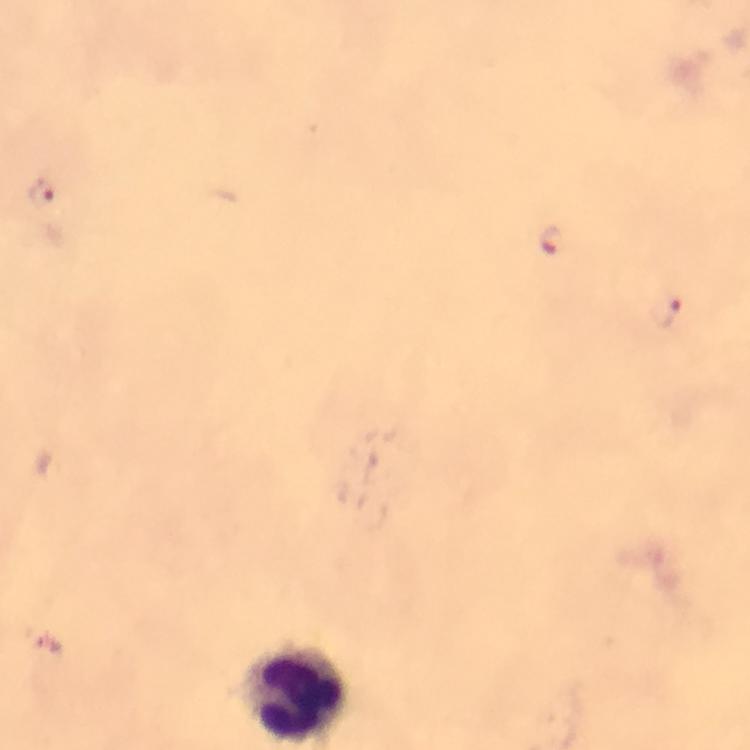

leukocyte locations = approximate object centers, in pixels from the top-left corner: (x=294, y=694)
magnification = 100x
immersion oil = used
Plasmodium parasite locations = approximate object centers, in pixels from the top-left corner: (x=40, y=190), (x=550, y=243), (x=666, y=310)
capture = smartphone photograph through a microscope
preparation = thick blood film
context = from a malaria diagnostic workup
stain = Giemsa
image size = 750×750 pixels
cropped from = a single field of view